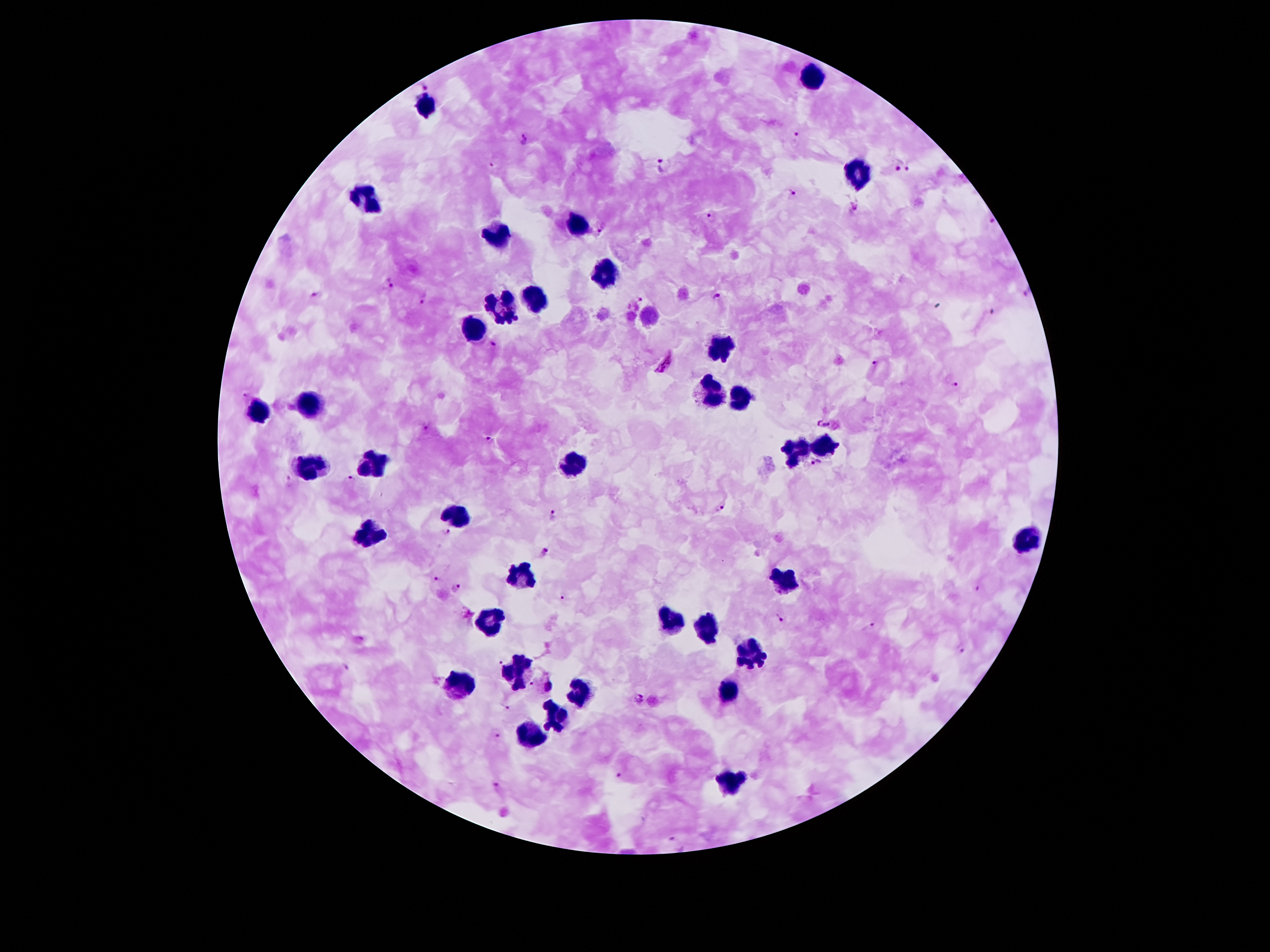

Approximate centers as (x, y) in pixels.
Summary:
  - Plasmodium parasite locations: (423, 83), (796, 137), (523, 138), (491, 162), (896, 165), (666, 166), (908, 166), (791, 197), (855, 206), (712, 215), (991, 221), (602, 229), (390, 282), (718, 294), (1027, 294), (314, 295), (426, 298), (638, 301), (994, 313), (492, 345), (664, 363), (874, 363), (954, 383), (243, 392), (825, 423), (426, 426), (489, 439), (816, 463), (349, 478), (288, 480), (721, 508), (554, 515), (447, 531), (544, 553), (436, 579), (977, 586), (457, 587), (564, 595), (780, 619), (868, 625), (960, 648), (500, 661), (532, 683), (550, 685), (639, 698), (508, 707), (496, 735), (619, 776), (496, 784), (674, 838)
  - Leukocyte locations: (814, 76), (425, 108), (861, 173), (366, 201), (577, 224), (500, 235), (605, 278), (502, 299), (534, 303), (475, 328), (723, 344), (711, 392), (737, 398), (307, 399), (260, 414), (825, 446), (796, 450), (375, 460), (577, 464), (312, 466), (459, 512), (371, 533), (1023, 537), (521, 576), (784, 578), (493, 616), (670, 621), (707, 628), (750, 653), (516, 673), (459, 685), (727, 689), (577, 691), (555, 712), (532, 737), (732, 780)
  - Patient malaria status: positive for Plasmodium falciparum
  - Image size: 1270×952 pixels
  - Capture: smartphone camera through the microscope eyepiece
  - Magnification: 100x
  - Stain: Giemsa
  - Preparation: thick blood film
  - Field of view: single